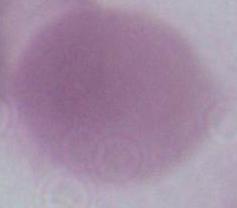
Captured at 1000x magnification. An erythrocyte is shown. Photomicrograph.